Name the blood parasite species.
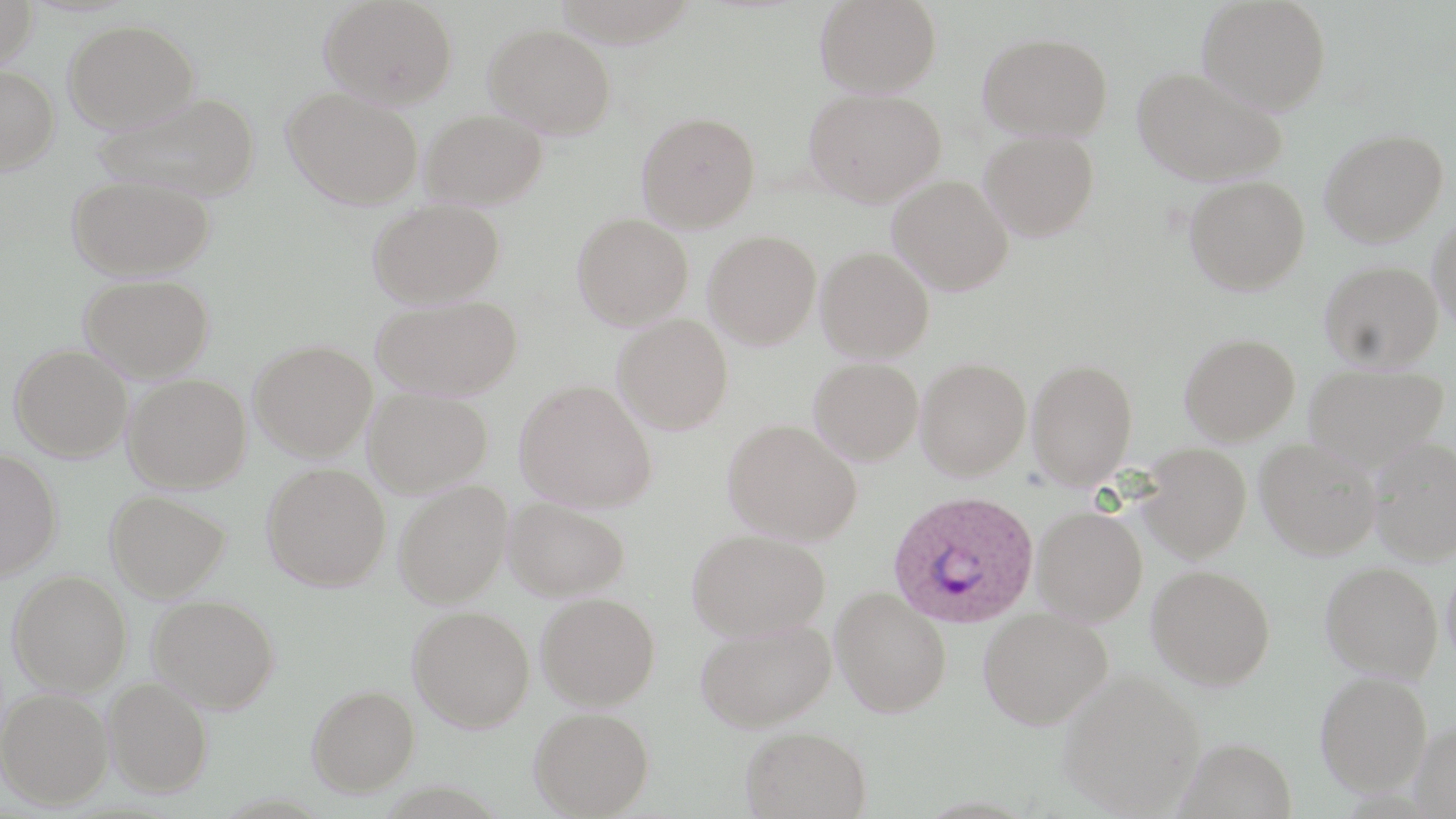

Plasmodium ovale.

Approximate bounding boxes as (x1, y1, x2, y2) in pixels. Uninfected red blood cell locations: (0, 0, 38, 68), (320, 0, 458, 109), (552, 0, 698, 47), (815, 0, 942, 96), (1197, 0, 1331, 115), (64, 19, 199, 132), (485, 24, 617, 138), (978, 32, 1113, 140), (0, 64, 59, 175), (1132, 66, 1288, 187), (804, 87, 947, 207), (283, 88, 423, 210), (95, 91, 262, 201), (421, 109, 548, 209), (636, 111, 760, 232), (1319, 128, 1448, 247), (979, 130, 1099, 241), (66, 174, 215, 280), (887, 176, 1014, 295), (1183, 176, 1310, 295), (369, 198, 505, 308), (572, 214, 693, 329), (1429, 214, 1456, 331), (703, 230, 822, 349), (815, 247, 934, 362), (1319, 260, 1443, 370), (79, 274, 215, 382), (371, 294, 523, 401), (613, 314, 734, 434), (1179, 332, 1300, 445), (249, 340, 377, 460), (9, 343, 132, 462), (809, 357, 923, 465), (916, 357, 1031, 480), (1026, 358, 1138, 489), (1304, 363, 1449, 468), (123, 374, 251, 493), (515, 379, 657, 512), (364, 387, 493, 497), (722, 419, 862, 545), (1370, 437, 1456, 563), (1255, 438, 1380, 559), (1138, 442, 1252, 562), (0, 448, 62, 581), (262, 463, 390, 591), (394, 480, 512, 608), (105, 490, 231, 602), (504, 497, 630, 601), (1031, 505, 1148, 626), (687, 528, 829, 641), (1320, 560, 1443, 682), (1147, 564, 1276, 690), (8, 570, 132, 695), (831, 587, 952, 717), (537, 592, 660, 709), (148, 594, 280, 713), (408, 606, 534, 731), (979, 607, 1113, 729), (695, 618, 836, 732), (1059, 669, 1206, 817), (1315, 670, 1433, 795), (104, 677, 213, 797), (306, 685, 420, 797), (1, 687, 112, 809), (529, 707, 654, 818), (1411, 720, 1456, 819), (740, 725, 871, 818), (1177, 737, 1297, 819). Plasmodium ovale-infected red blood cell locations: (887, 489, 1039, 629). One field of a larger specimen. Thin blood smear. 1000x magnification. Image is 1456×819 pixels. May-Grünwald-Giemsa stain. Optical microscopy.